Describe the morphology of the erythrocytes.
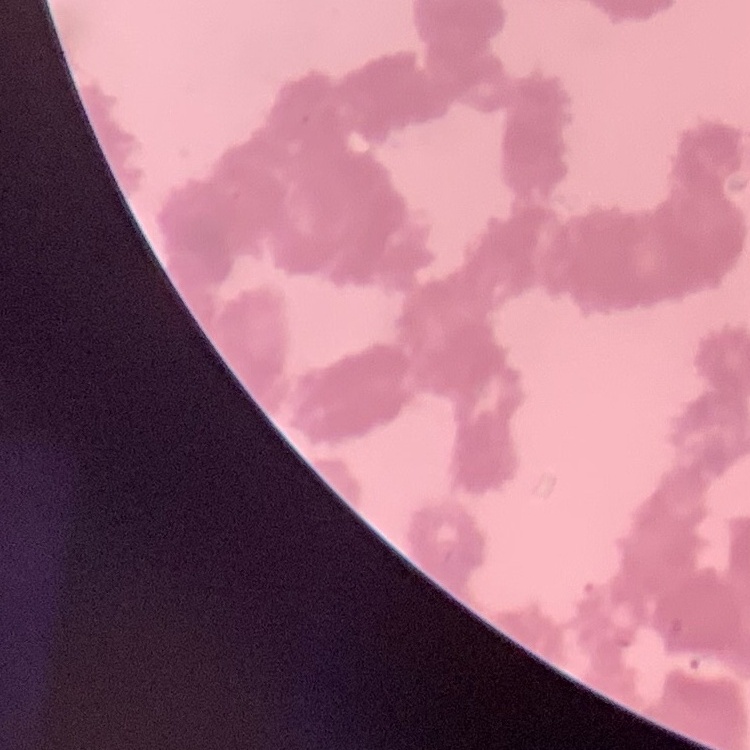
They show rouleaux formation.

Square crop of a larger photomicrograph. Thin blood film. Stained with either Field's or Giemsa.